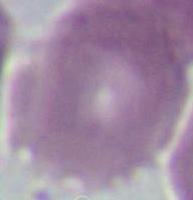

identification = erythrocyte
modality = micrograph
magnification = 1000x